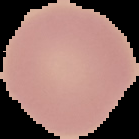

Summary:
  - Image type: segmented cell region on a black background
  - Preparation: thin blood film
  - Result: no Plasmodium parasites seen
  - Image size: 139×139 pixels